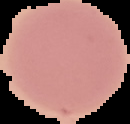

From a thin blood smear. Result: no Plasmodium parasites detected. Image is 130×124 pixels. Cell region segmented out of the field of view; the surrounding area is masked to black.